Comment on the morphology of the erythrocytes.
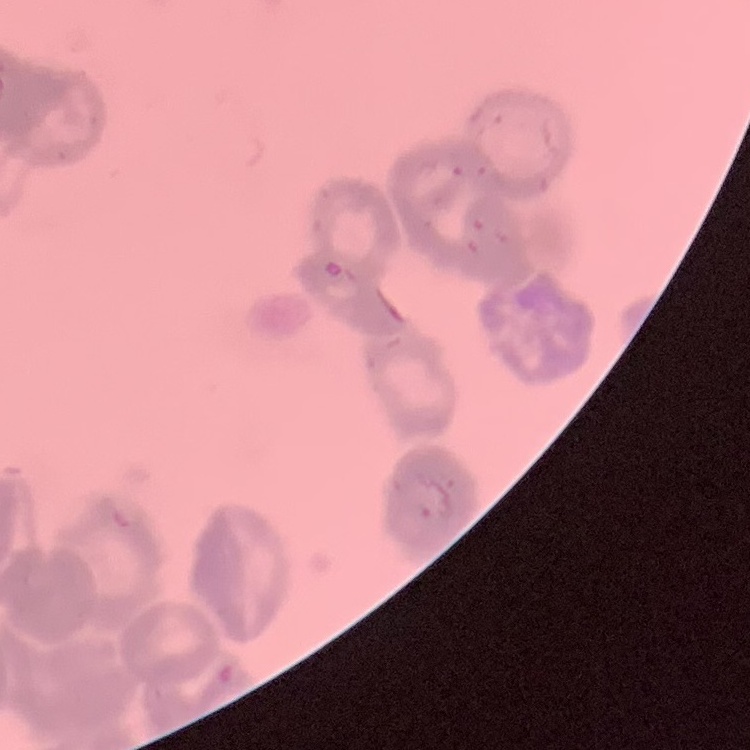
They show rouleaux formation.

image type = one tile cut from a larger photomicrograph
preparation = thin peripheral smear
stain = Field's or Giemsa